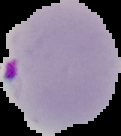 Cell region segmented out of the field of view; the surrounding area is masked to black. Image is 121×136 pixels. Result: Plasmodium parasites identified. From a thin blood film.